Identify the parasite.
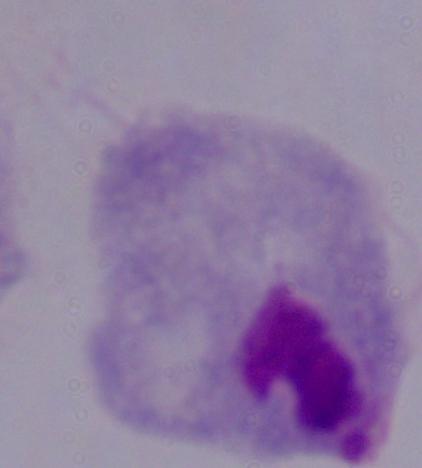
A trichomonad.

Photomicrograph. 1000x magnification.